Name the blood parasite species.
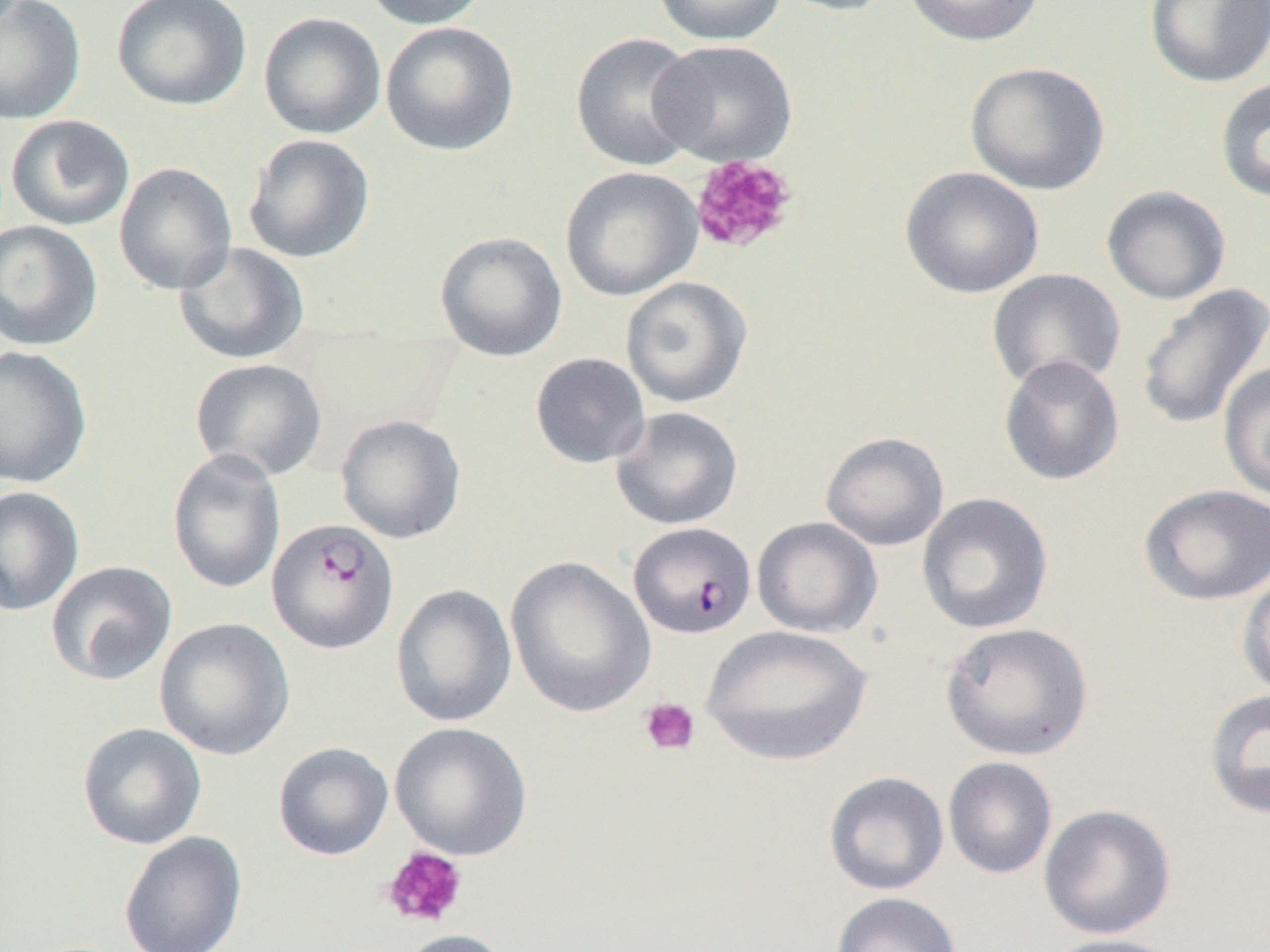

Plasmodium falciparum.

Approximate bounding boxes as named x1/y1/x2/y2 corners in pixels. Uninfected red blood cell locations: (x1=0, y1=0, x2=87, y2=125), (x1=111, y1=0, x2=252, y2=111), (x1=359, y1=0, x2=492, y2=30), (x1=652, y1=0, x2=786, y2=45), (x1=772, y1=0, x2=898, y2=17), (x1=902, y1=0, x2=1047, y2=46), (x1=1145, y1=0, x2=1270, y2=89), (x1=258, y1=12, x2=387, y2=140), (x1=380, y1=21, x2=520, y2=157), (x1=570, y1=32, x2=705, y2=171), (x1=651, y1=39, x2=798, y2=167), (x1=965, y1=61, x2=1110, y2=195), (x1=1214, y1=77, x2=1270, y2=204), (x1=5, y1=114, x2=136, y2=232), (x1=243, y1=134, x2=376, y2=264), (x1=113, y1=161, x2=238, y2=295), (x1=560, y1=166, x2=703, y2=301), (x1=900, y1=166, x2=1044, y2=299), (x1=1101, y1=185, x2=1231, y2=304), (x1=0, y1=220, x2=103, y2=351), (x1=434, y1=231, x2=568, y2=362), (x1=173, y1=242, x2=310, y2=365), (x1=987, y1=269, x2=1125, y2=392), (x1=620, y1=276, x2=754, y2=408), (x1=1135, y1=283, x2=1270, y2=432), (x1=0, y1=345, x2=93, y2=488), (x1=530, y1=352, x2=651, y2=469), (x1=999, y1=354, x2=1124, y2=485), (x1=189, y1=357, x2=327, y2=481), (x1=1217, y1=361, x2=1270, y2=502), (x1=610, y1=407, x2=743, y2=530), (x1=335, y1=413, x2=467, y2=544), (x1=820, y1=431, x2=949, y2=551), (x1=167, y1=446, x2=287, y2=595), (x1=1139, y1=485, x2=1270, y2=605), (x1=0, y1=486, x2=84, y2=617), (x1=917, y1=492, x2=1053, y2=634), (x1=752, y1=516, x2=883, y2=637), (x1=505, y1=556, x2=655, y2=718), (x1=45, y1=560, x2=177, y2=686), (x1=1237, y1=568, x2=1270, y2=700), (x1=390, y1=584, x2=517, y2=727), (x1=154, y1=617, x2=295, y2=761), (x1=940, y1=622, x2=1093, y2=761), (x1=701, y1=624, x2=871, y2=765), (x1=1203, y1=688, x2=1270, y2=820), (x1=389, y1=721, x2=533, y2=861), (x1=77, y1=722, x2=207, y2=850), (x1=272, y1=742, x2=394, y2=861), (x1=943, y1=757, x2=1057, y2=879), (x1=824, y1=771, x2=949, y2=895), (x1=1039, y1=804, x2=1175, y2=939), (x1=118, y1=831, x2=248, y2=952), (x1=830, y1=892, x2=962, y2=952), (x1=393, y1=928, x2=514, y2=952), (x1=1044, y1=934, x2=1189, y2=952). Platelet locations: (x1=689, y1=154, x2=798, y2=255), (x1=639, y1=698, x2=700, y2=756), (x1=379, y1=845, x2=469, y2=929). Plasmodium falciparum-infected red blood cell locations: (x1=267, y1=517, x2=399, y2=654), (x1=628, y1=522, x2=756, y2=638). One field of a larger specimen. Image is 1270×952 pixels. 1000x magnification. Light microscopy. Thin blood smear.